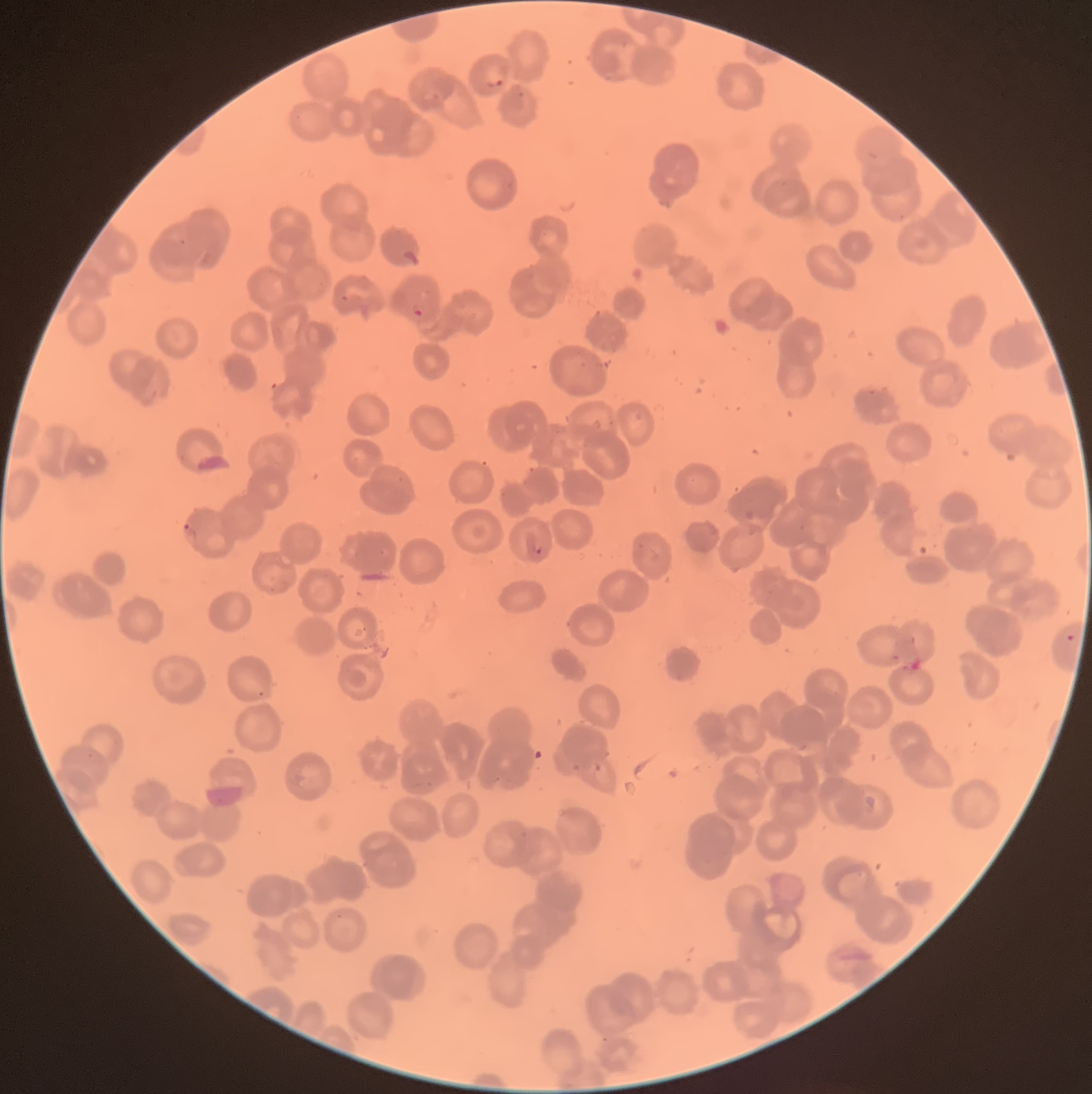 Approximate bounding boxes as (x1, y1, x2, y2) in pixels. Plasmodium parasite locations: (485, 75, 505, 90), (515, 90, 527, 100), (403, 248, 422, 266), (340, 294, 350, 303), (411, 307, 424, 319), (182, 523, 198, 543), (532, 542, 545, 555), (1064, 633, 1077, 644), (256, 690, 266, 698), (86, 751, 95, 759). Image is 1092×1094 pixels. The red blood cells show rouleaux formation. Optical microscopy. Thin blood smear.